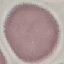

Summary:
  - Result: no malaria parasites detected
  - Image type: cell patch, automatically extracted from a larger field of view and resized to 64 × 64 pixels
  - Preparation: thin blood film
  - Capture: smartphone through the microscope eyepiece
  - Stain: Giemsa